Name the parasite shown.
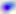

Toxoplasma gondii.

Photomicrograph. 400x magnification.